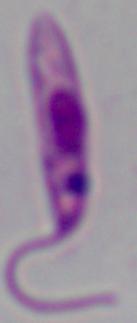
modality = micrograph
magnification = 1000x
identification = Leishmania